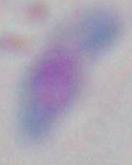

Toxoplasma gondii is shown. Photomicrograph. Captured at 1000x magnification.